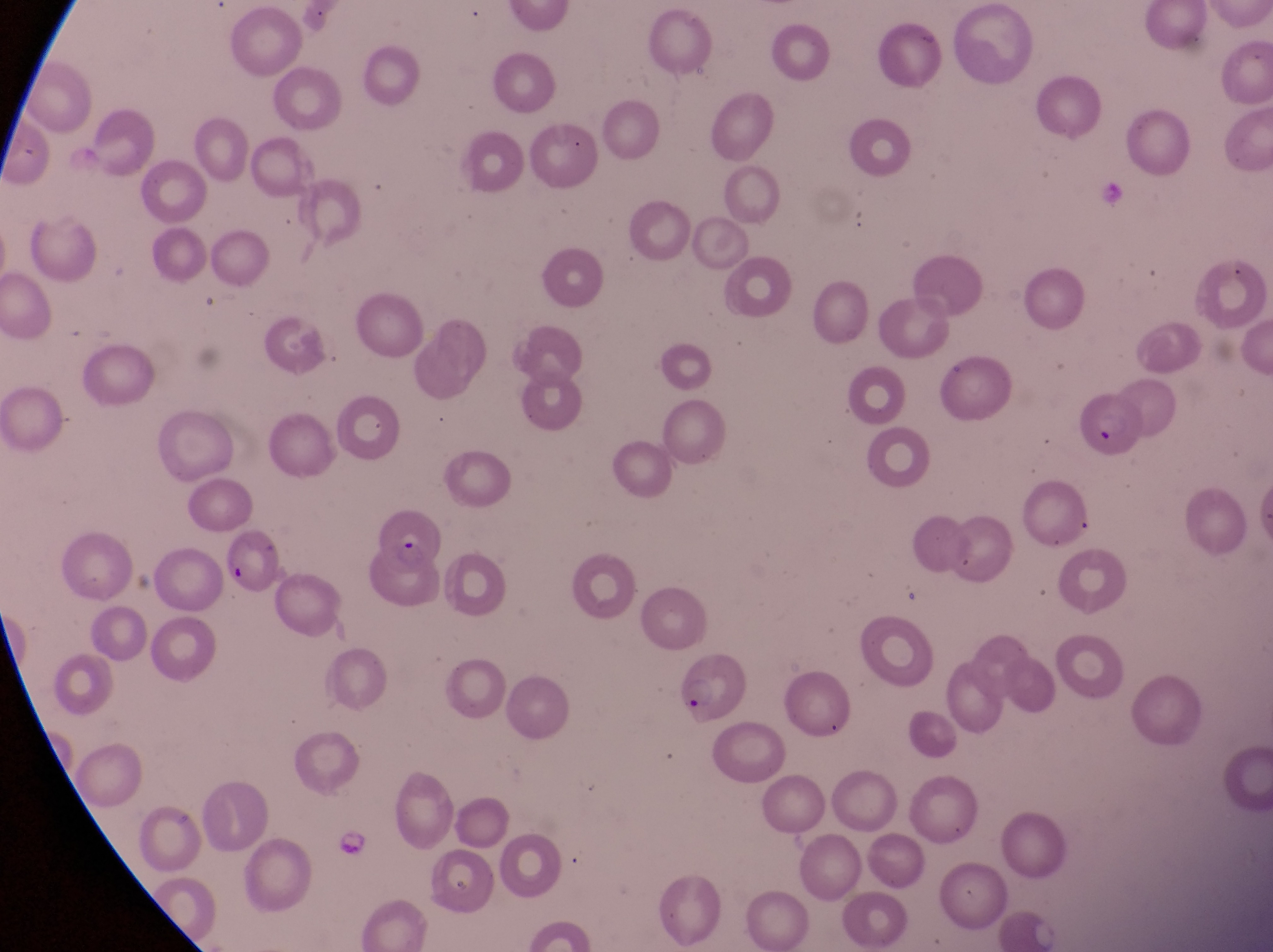
magnification = 1000x
image size = 1273×952 pixels
parasitised red blood cell locations = approximate bounding boxes as [left, top, right, bottom] in pixels: [1071, 394, 1143, 466], [379, 512, 446, 577], [671, 654, 745, 729]
preparation = thin blood smear
capture = smartphone photograph through the eyepiece of an Olympus CX-23 microscope
artifact (platelet-like body, stain precipitate, or debris) locations = approximate bounding boxes as [left, top, right, bottom] in pixels: [222, 557, 255, 592]
country = Uganda
field of view = single